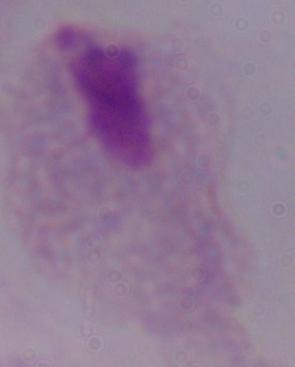
Summary:
  - Modality: micrograph
  - Identification: trichomonad
  - Magnification: 1000x